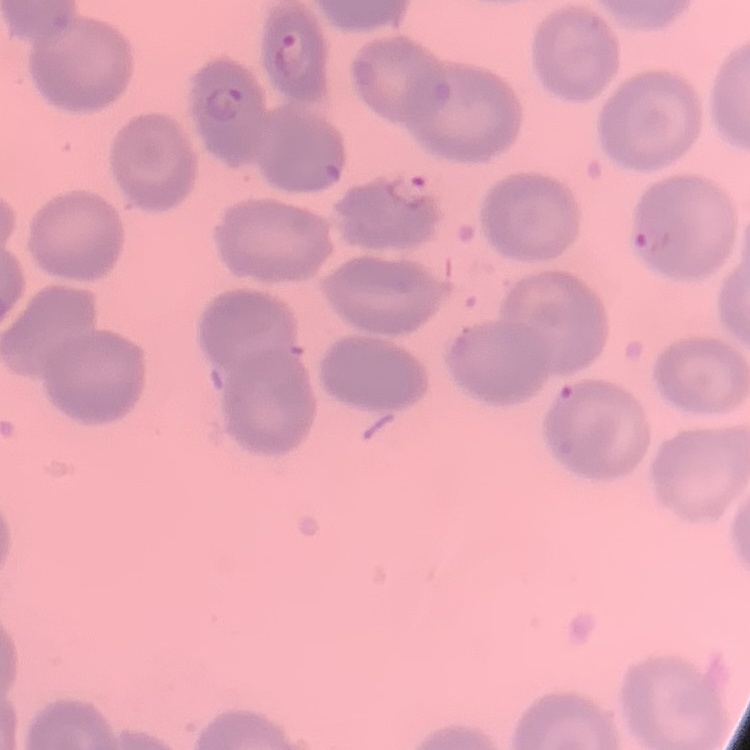

erythrocyte_morphology: no rouleaux formation
stain: Field's or Giemsa
preparation: thin peripheral smear
image_type: square crop of a larger photomicrograph